Assess this cell for malaria.
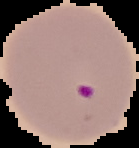
It is parasitized.

Summary:
  - Image size: 139×148 pixels
  - Image type: segmented cell region on a black background
  - Preparation: thin blood film